Report the malaria status of this cell.
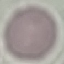

Uninfected.

Cell patch, automatically extracted from a larger field of view and resized to 64 × 64 pixels. Acquired by smartphone through the microscope eyepiece. Thin smear of blood. Giemsa-stained preparation.